State which parasite is depicted.
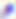
This is Toxoplasma gondii.

Captured at 400x magnification. Photomicrograph.